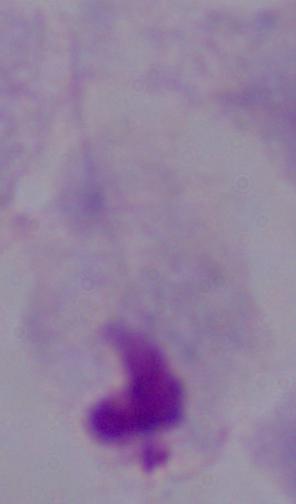
modality: photomicrograph
magnification: 1000x
identification: trichomonad